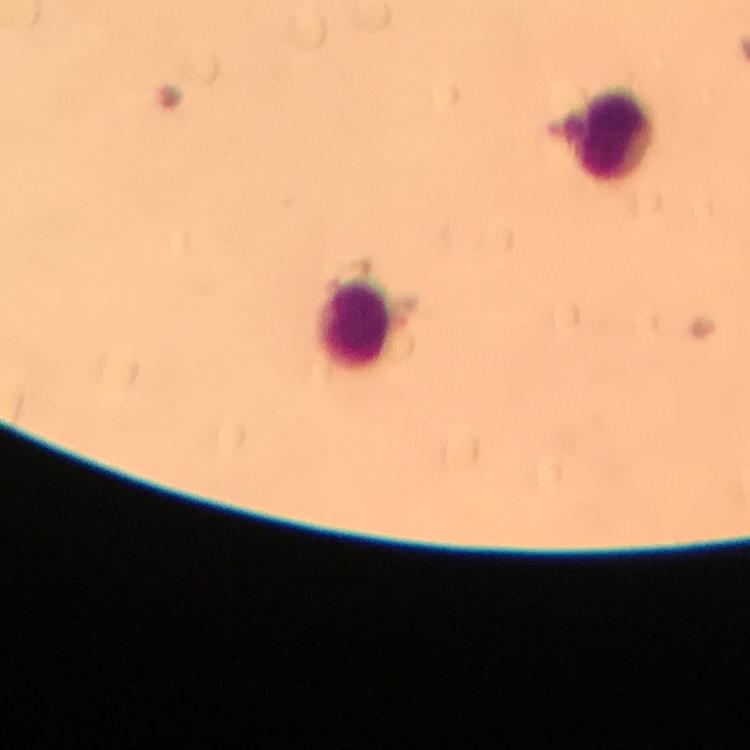

Approximate centers as {x, y} in pixels.
Summary:
  - Leukocyte locations: {609, 132}, {357, 323}
  - Stain: Giemsa
  - Cropped from: one field of view
  - Plasmodium parasites: none seen
  - Image size: 750×750 pixels
  - Capture: smartphone camera through the microscope
  - Preparation: thick blood film
  - Immersion oil: applied
  - Context: from a diagnostic examination for malaria
  - Magnification: 100x